Classify this cell by malaria status.
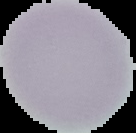

It is uninfected.

From a thin blood smear. Segmented cell region on a black background. Image is 136×133 pixels.